Comment on the morphology of the red blood cells.
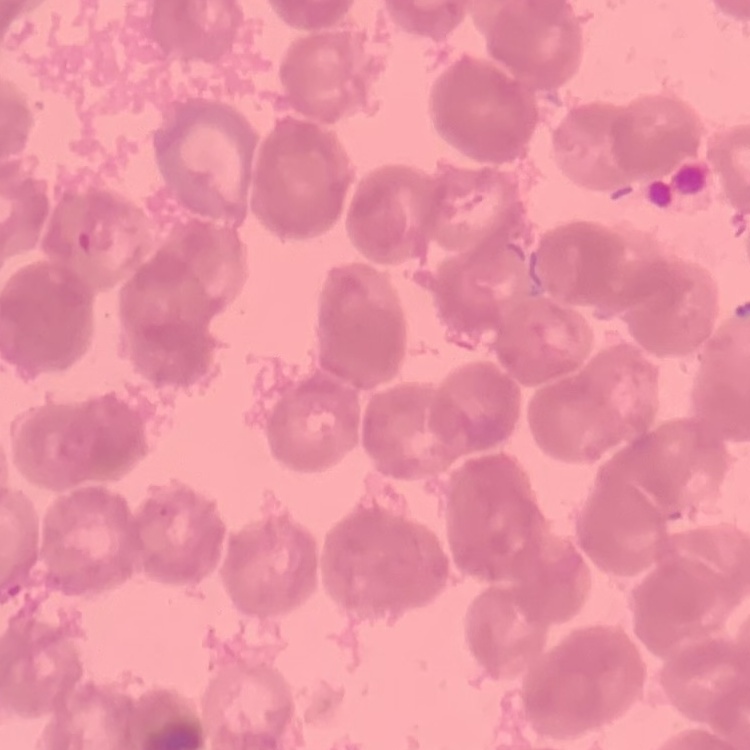

Rouleaux formation.

image_type: one tile cut from a larger photomicrograph
stain: Field's or Giemsa
preparation: thin peripheral smear